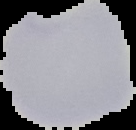
{
  "image_type": "cell region segmented out of the field of view; surrounding area masked to black",
  "preparation": "thin blood smear",
  "malaria_status": "parasitized",
  "image_size": "136×130 pixels"
}